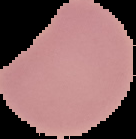
malaria status = uninfected
preparation = thin blood film
image size = 136×139 pixels
image type = cell region segmented out of the field of view; surrounding area masked to black